Outline each uninfected red blood cell.
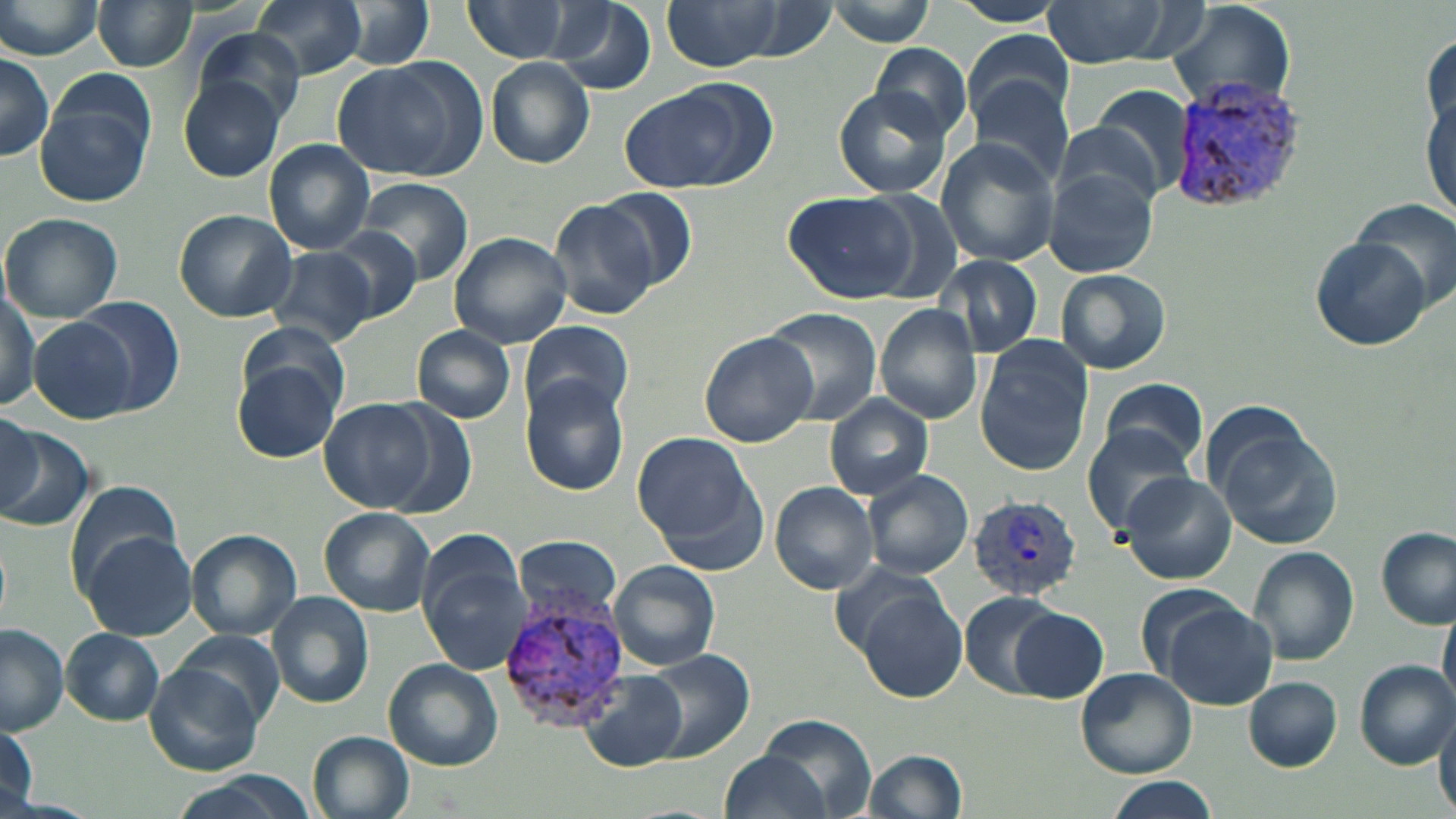
Approximate bounding boxes as (x1,y1)-(x2,y2) corner pairs in pixels.
Uninfected red blood cells: (251,0)-(369,79), (550,0)-(655,94), (0,1)-(106,60), (93,1)-(197,72), (459,1)-(581,63), (664,1)-(787,71), (1041,1)-(1169,67), (828,2)-(938,46), (1165,2)-(1295,114), (948,3)-(1067,27), (333,5)-(437,72), (192,26)-(306,124), (964,29)-(1076,121), (869,42)-(975,142), (0,52)-(54,162), (332,56)-(488,181), (485,58)-(594,169), (176,76)-(287,183), (39,77)-(153,204), (972,78)-(1075,189), (617,82)-(772,194), (833,86)-(953,200), (1089,87)-(1198,201), (1420,95)-(1454,223), (934,138)-(1060,268), (264,139)-(375,254), (1045,166)-(1157,280), (356,177)-(474,283), (595,189)-(699,293), (782,192)-(924,305), (550,198)-(663,322), (1352,198)-(1454,308), (174,209)-(297,321), (2,213)-(123,323), (322,224)-(422,324), (447,231)-(572,350), (1310,235)-(1432,350), (267,246)-(375,346), (935,258)-(1043,356), (1056,268)-(1170,376), (0,287)-(42,411), (69,296)-(185,416), (874,304)-(985,424), (0,306)-(96,413), (762,310)-(881,422), (29,318)-(138,425), (519,320)-(634,422), (241,321)-(351,409), (411,326)-(516,422), (699,332)-(818,446), (974,341)-(1093,476), (234,359)-(342,463), (520,377)-(628,495), (1098,378)-(1207,474), (826,394)-(933,499), (379,397)-(478,517), (319,399)-(438,513), (0,418)-(89,530), (0,418)-(44,514), (1083,426)-(1191,532), (1221,429)-(1344,550), (631,433)-(762,560), (861,468)-(974,579), (1118,471)-(1236,586), (65,480)-(182,589), (771,481)-(878,595), (319,507)-(436,616), (1376,527)-(1454,629), (187,530)-(301,639), (79,531)-(197,640), (514,534)-(622,622), (419,544)-(535,676), (1247,545)-(1359,666), (608,559)-(721,672), (827,561)-(954,662), (854,591)-(969,703), (960,591)-(1066,697), (267,592)-(372,709), (1440,600)-(1456,708), (1163,604)-(1278,711), (1008,606)-(1109,702), (0,625)-(69,734), (61,628)-(164,725), (172,629)-(286,727), (648,652)-(754,763), (1355,659)-(1455,768), (148,660)-(267,776), (384,660)-(504,769), (1076,669)-(1196,778), (580,670)-(689,770), (1245,677)-(1342,770), (1436,702)-(1456,815), (758,716)-(875,819), (1,723)-(37,810), (309,732)-(416,819), (720,748)-(834,819), (861,749)-(967,819), (163,773)-(308,819), (1102,777)-(1219,819).

Plasmodium vivax-infected red blood cell locations: (1177,75)-(1302,210), (966,492)-(1083,598), (503,599)-(630,726). Slide-level diagnosis: Plasmodium vivax. Image is 1456×819 pixels. Thin blood film. One field of a larger specimen. Captured at 1000x magnification. Light microscopy. May-Grünwald-Giemsa-stained preparation.